Locate every blood parasite and identify its species.
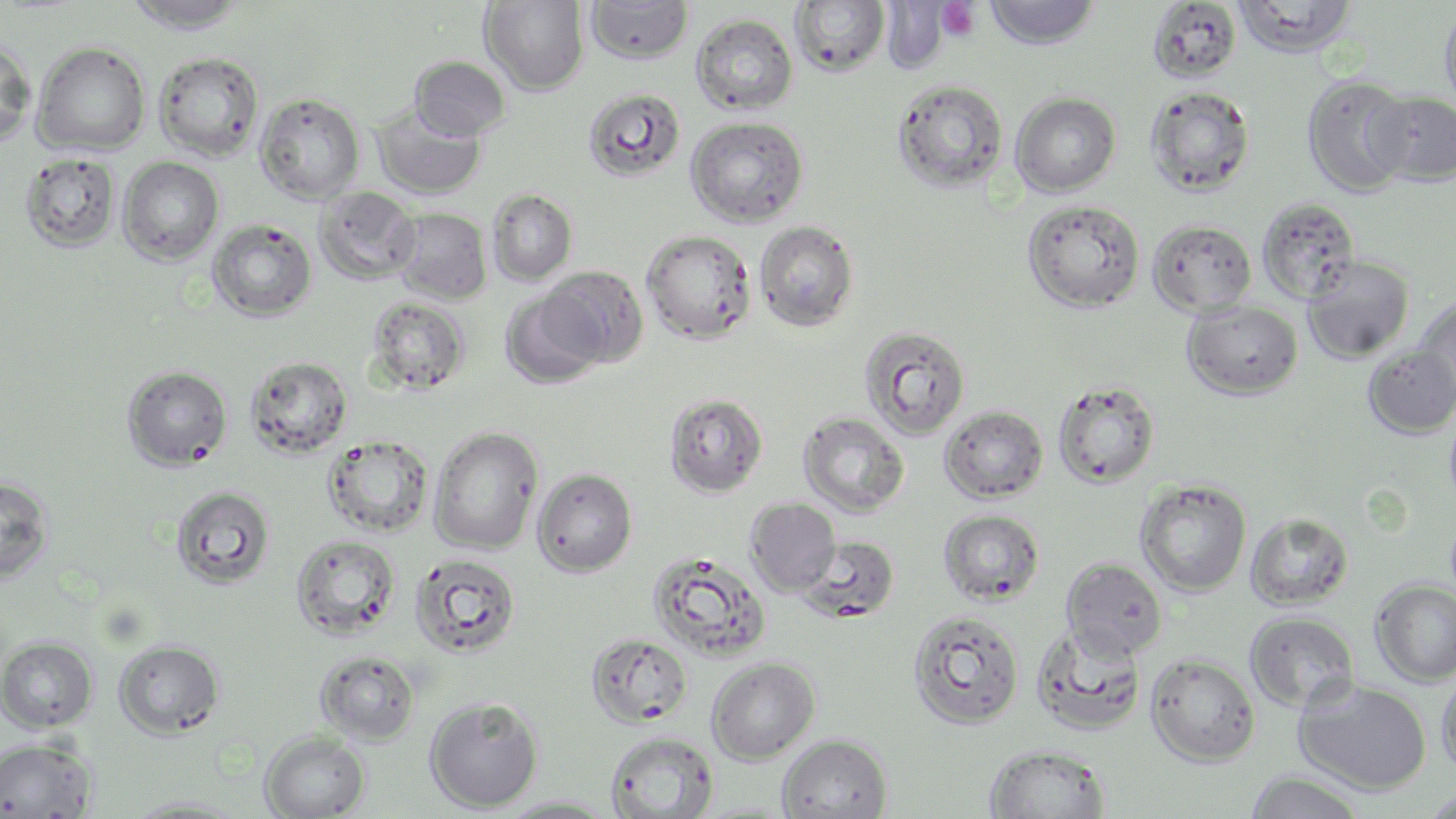
No blood parasites observed.

slide_level_diagnosis: negative for blood parasites
stain: May-Grünwald-Giemsa
uninfected_red_blood_cell_locations: 'approximate bounding boxes as [x1, y1, x2, y2] in pixels: [585, 0, 694, 64], [984, 0, 1100, 49], [120, 1, 252, 34], [479, 1, 590, 94], [789, 1, 890, 78], [1233, 1, 1357, 57], [1147, 2, 1242, 84], [1439, 2, 1456, 118], [690, 13, 798, 116], [0, 38, 37, 149], [30, 41, 151, 157], [153, 52, 264, 162], [410, 56, 510, 140], [1302, 74, 1414, 197], [892, 78, 1009, 193], [1145, 86, 1256, 197], [583, 88, 686, 183], [1369, 91, 1456, 188], [255, 92, 366, 204], [1010, 92, 1121, 197], [373, 104, 486, 200], [685, 116, 808, 227], [19, 152, 121, 253], [118, 157, 224, 265], [314, 186, 421, 285], [486, 188, 577, 285], [1256, 196, 1361, 305], [1022, 199, 1145, 313], [391, 207, 492, 305], [207, 219, 317, 321], [1147, 219, 1257, 318], [753, 220, 860, 333], [640, 228, 757, 344], [1302, 255, 1415, 364], [541, 266, 649, 367], [500, 289, 607, 389], [1411, 295, 1456, 406], [366, 296, 472, 394], [1182, 300, 1304, 400], [858, 325, 972, 440], [1362, 345, 1456, 439], [245, 355, 353, 459], [121, 364, 233, 471], [1052, 380, 1161, 489], [664, 393, 768, 498], [1443, 401, 1456, 515], [939, 405, 1049, 503], [799, 411, 910, 518], [429, 426, 543, 554], [323, 436, 433, 538], [533, 468, 637, 577], [0, 475, 55, 585], [1135, 479, 1252, 596], [169, 485, 277, 590], [745, 497, 840, 594], [938, 509, 1045, 606], [1245, 511, 1353, 610], [290, 533, 401, 641], [797, 535, 900, 622], [646, 550, 772, 663], [409, 553, 522, 659], [1061, 557, 1168, 660], [1370, 579, 1456, 686], [908, 609, 1025, 729], [1244, 611, 1359, 713], [1030, 622, 1146, 736], [586, 632, 692, 729], [1, 636, 98, 734], [113, 639, 225, 738], [315, 650, 420, 745], [1145, 653, 1260, 766], [706, 657, 820, 764], [1436, 668, 1456, 778], [1295, 679, 1432, 795], [425, 696, 544, 813], [260, 731, 370, 818], [605, 731, 718, 818], [777, 733, 892, 818], [0, 737, 97, 817], [985, 743, 1110, 818], [1244, 770, 1368, 818], [1418, 787, 1456, 818], [124, 795, 251, 817], [495, 795, 621, 817]'
modality: light microscopy
platelet_locations: 'approximate bounding boxes as [x1, y1, x2, y2] in pixels: [937, 2, 981, 42]'
magnification: 1000x
preparation: thin blood smear
image_size: 1456×819 pixels
field_of_view: single